Outline each Plasmodium ovale-infected red blood cell.
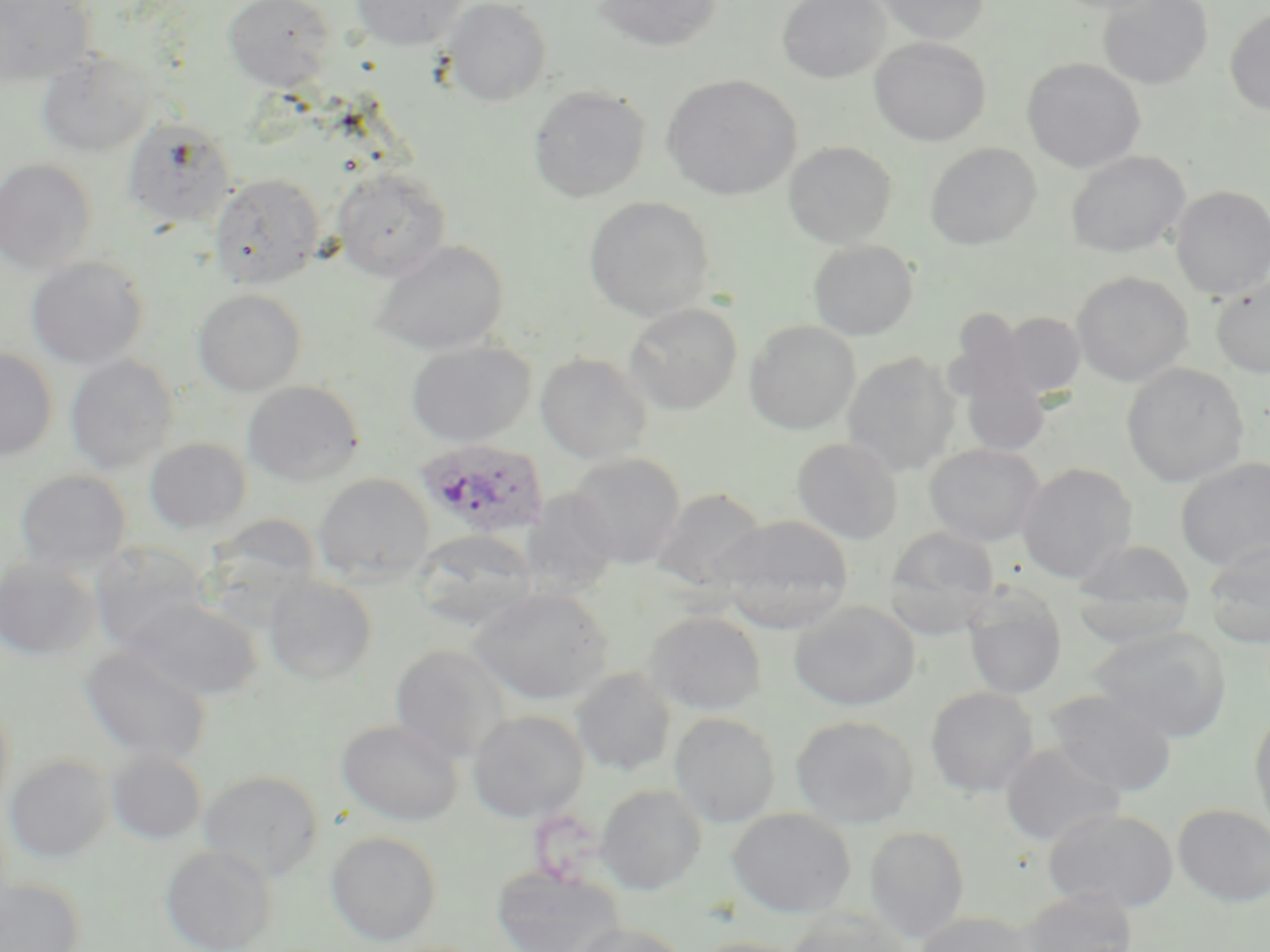
Approximate bounding boxes as (x1,y1)-(x2,y2) corner pairs in pixels.
Plasmodium ovale-infected red blood cells: (415,437)-(550,540).

Uninfected red blood cell locations: (223,0)-(335,90), (351,0)-(468,51), (442,0)-(552,107), (594,0)-(722,52), (777,0)-(889,83), (871,0)-(991,44), (1050,0)-(1168,15), (1098,0)-(1213,90), (0,1)-(95,87), (1224,8)-(1270,116), (871,37)-(991,146), (35,51)-(156,157), (1022,58)-(1145,172), (662,74)-(802,201), (528,86)-(650,203), (123,116)-(236,229), (783,141)-(897,248), (925,142)-(1042,249), (1066,151)-(1190,258), (0,159)-(97,274), (332,167)-(452,281), (209,173)-(325,289), (1170,186)-(1270,299), (583,196)-(715,321), (808,239)-(919,340), (372,240)-(509,355), (26,256)-(149,369), (1072,271)-(1194,387), (1211,276)-(1270,378), (193,289)-(306,396), (624,302)-(742,415), (942,312)-(1037,408), (996,312)-(1085,398), (744,320)-(861,435), (405,340)-(537,447), (0,347)-(58,462), (842,351)-(961,477), (535,353)-(653,464), (65,355)-(177,474), (1122,362)-(1249,487), (958,371)-(1050,457), (241,380)-(365,486), (791,437)-(903,544), (143,438)-(252,534), (924,443)-(1045,547), (567,453)-(686,569), (1176,457)-(1269,571), (1016,462)-(1137,584), (14,469)-(132,573), (313,473)-(435,586), (650,487)-(769,592), (518,488)-(620,599), (205,513)-(322,618), (715,515)-(855,632), (883,526)-(1000,635), (414,529)-(537,630), (1071,539)-(1196,646), (1201,539)-(1270,647), (87,543)-(212,654), (0,556)-(101,661), (263,574)-(378,684), (961,585)-(1068,701), (469,586)-(615,705), (124,597)-(261,701), (789,600)-(920,711), (644,609)-(767,715), (1087,626)-(1231,742), (390,643)-(510,763), (80,644)-(214,765), (571,668)-(677,776), (925,686)-(1039,797), (1044,688)-(1177,796), (0,693)-(15,818), (1250,708)-(1270,837), (468,710)-(589,823), (669,712)-(780,827), (791,714)-(918,829), (336,719)-(464,826), (1001,743)-(1125,846), (106,750)-(207,844), (5,755)-(114,863), (199,769)-(325,882), (596,784)-(707,895), (1173,804)-(1270,906), (727,807)-(857,918), (1042,807)-(1179,913), (865,826)-(970,942), (326,830)-(442,945), (160,845)-(276,952), (491,867)-(627,952), (0,878)-(85,952), (1017,889)-(1140,952), (785,907)-(911,952), (914,911)-(1036,952), (570,922)-(690,952), (689,936)-(809,952). Slide-level diagnosis: Plasmodium ovale. Light microscopy. Captured at 1000x magnification. May-Grünwald-Giemsa-stained preparation. Single field of view. Image is 1270×952 pixels. Thin blood smear.